Identify the cell.
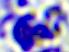

This is a leukocyte.

Summary:
  - Modality: micrograph
  - Magnification: 400x